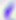

Summary:
  - Magnification: 400x
  - Modality: photomicrograph
  - Identification: Toxoplasma gondii